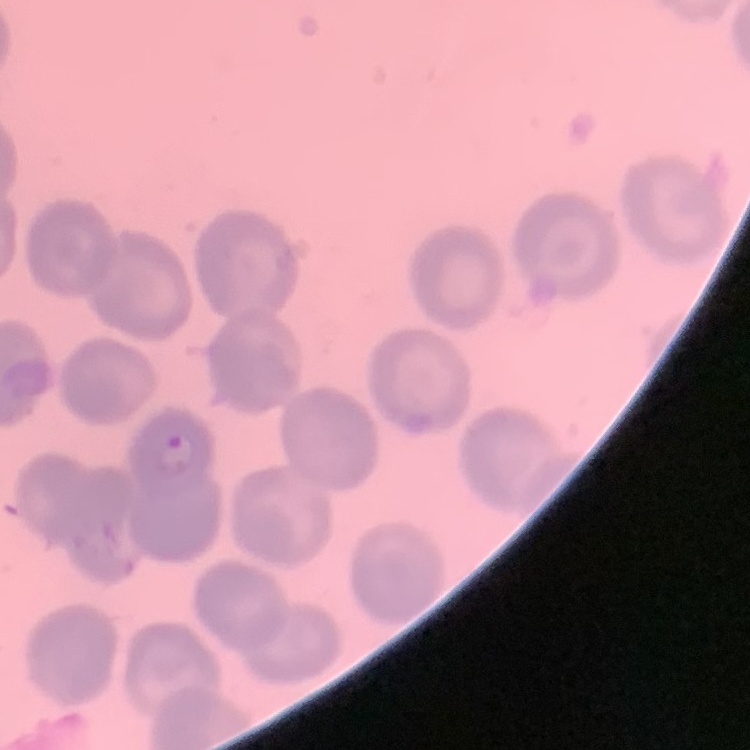

Summary:
  - Erythrocyte morphology: no rouleaux formation
  - Stain: Field's or Giemsa
  - Image type: square crop of a larger photomicrograph
  - Preparation: thin blood film